Give the position of every leukocyte visible.
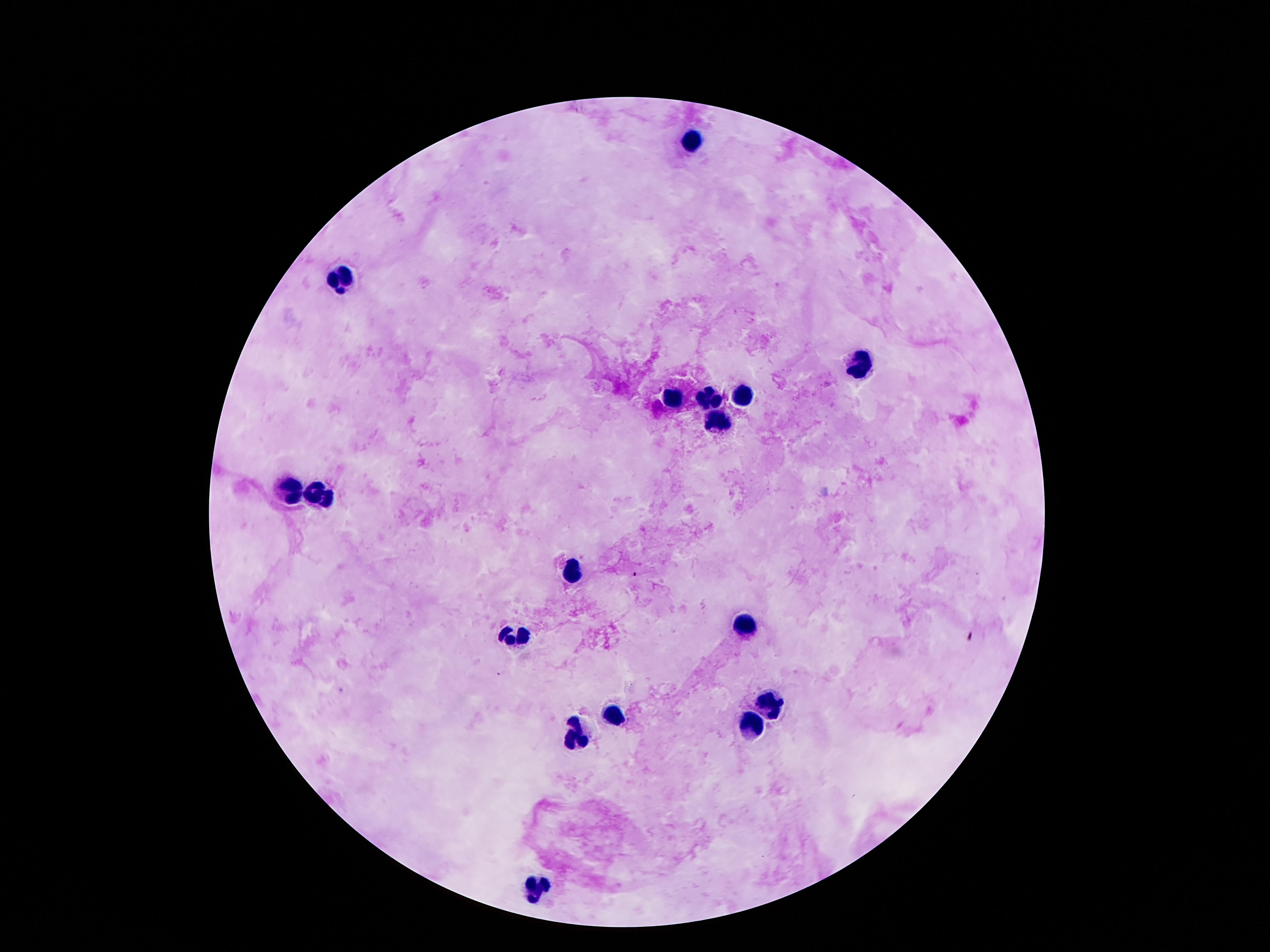
Approximate centers as [x, y] in pixels.
Leukocytes: [693, 140], [344, 278], [861, 363], [744, 395], [673, 399], [708, 400], [715, 423], [294, 490], [323, 492], [574, 572], [745, 626], [516, 637], [770, 706], [616, 717], [752, 726], [575, 738], [539, 888].

stain: Giemsa
capture: smartphone camera through the microscope eyepiece
preparation: thick blood smear
image_size: 1270×952 pixels
field_of_view: one from this slide
patient_malaria_status: negative
magnification: 100x